Assess this cell for malaria.
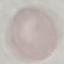
It is uninfected.

Cell patch, automatically extracted from a larger field of view and resized to 64 × 64 pixels. Thin smear of blood. Giemsa-stained preparation. Photographed with a smartphone camera at the microscope eyepiece.